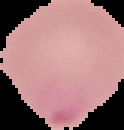

{
  "malaria_status": "parasitized",
  "image_type": "segmented cell region on a black background",
  "preparation": "thin blood film",
  "image_size": "124×130 pixels"
}